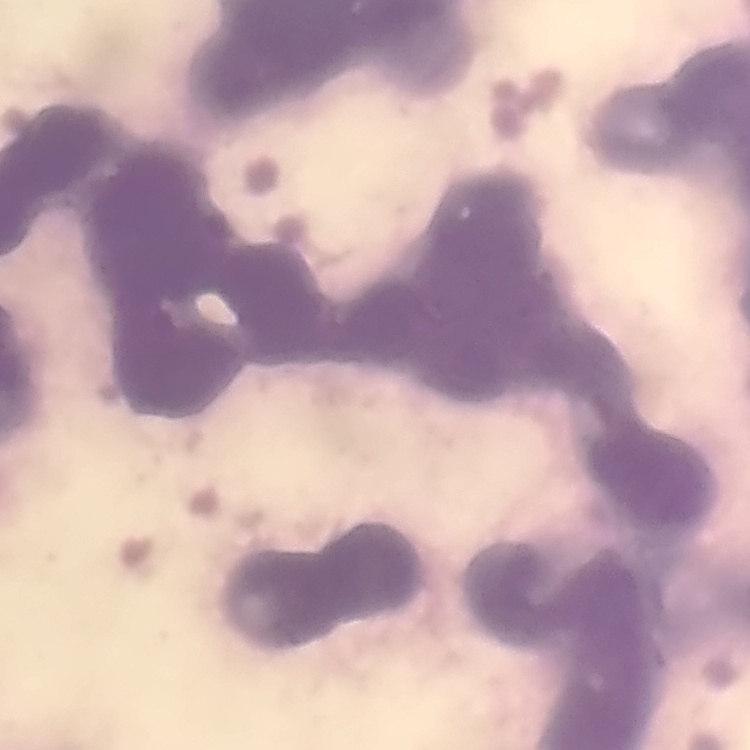
Summary:
  - Erythrocyte morphology: rouleaux formation
  - Preparation: thin peripheral smear
  - Stain: Field's or Giemsa
  - Image type: one tile cut from a larger photomicrograph